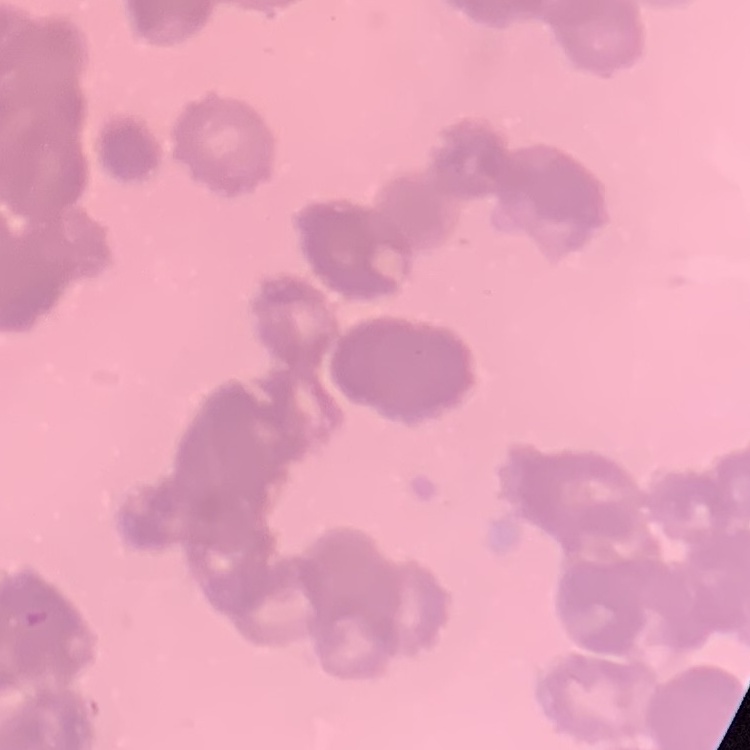

{
  "red_blood_cell_morphology": "rouleaux formation",
  "preparation": "thin peripheral smear",
  "image_type": "square crop of a larger photomicrograph",
  "stain": "Field's or Giemsa"
}